Identify the cell.
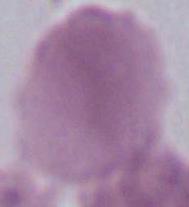
This is an erythrocyte.

1000x magnification. Micrograph.